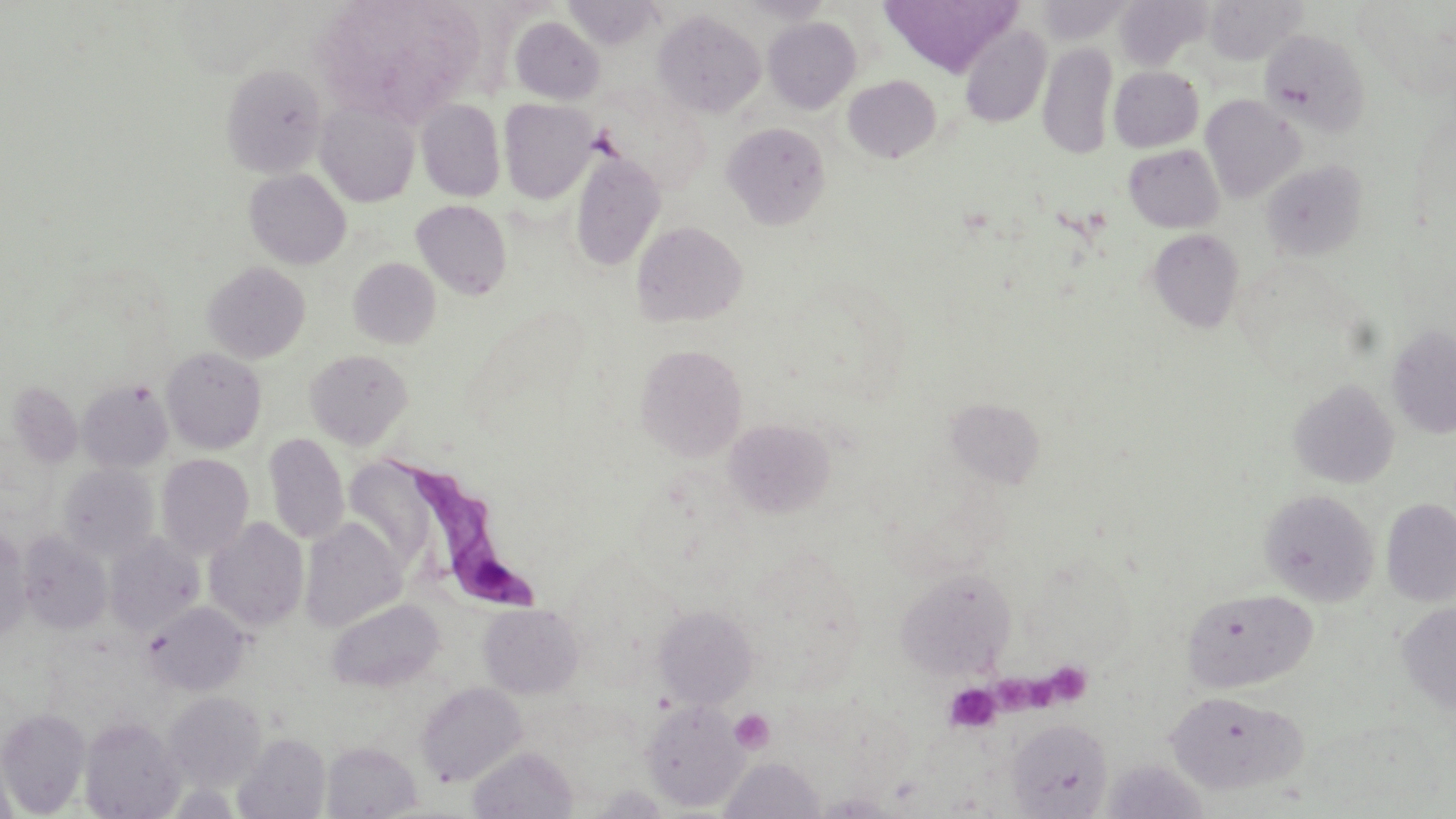
Summary:
  - Coordinate format: approximate bounding boxes as (x1, y1, x2, y2) in pixels
  - Platelet locations: (1052, 671, 1085, 707), (1000, 675, 1063, 725), (943, 683, 1001, 733), (729, 709, 774, 754)
  - Uninfected red blood cell locations: (312, 0, 485, 125), (879, 0, 1021, 77), (1114, 0, 1208, 71), (1205, 0, 1304, 64), (1035, 1, 1131, 43), (653, 10, 766, 118), (509, 16, 605, 104), (763, 17, 861, 113), (959, 23, 1052, 127), (1259, 29, 1371, 138), (1038, 42, 1118, 160), (220, 64, 327, 178), (1109, 66, 1204, 151), (843, 75, 941, 164), (1200, 94, 1306, 203), (315, 99, 420, 207), (416, 99, 505, 201), (499, 99, 598, 203), (722, 122, 831, 230), (1124, 144, 1224, 233), (569, 150, 666, 271), (1261, 160, 1366, 261), (244, 168, 351, 269), (411, 200, 512, 300), (631, 221, 747, 326), (1147, 229, 1244, 333), (349, 257, 441, 349), (203, 261, 311, 362), (1386, 324, 1456, 439), (635, 344, 748, 462), (161, 347, 267, 454), (304, 349, 413, 449), (79, 379, 173, 473), (1288, 379, 1399, 488), (7, 381, 83, 467), (945, 398, 1044, 489), (724, 418, 835, 518), (264, 432, 349, 546), (156, 454, 254, 559), (349, 459, 430, 569), (57, 463, 159, 561), (1259, 489, 1379, 605), (1382, 498, 1456, 607), (204, 517, 309, 631), (300, 517, 406, 632), (0, 531, 31, 639), (18, 532, 112, 634), (105, 532, 204, 636), (895, 568, 1016, 679), (1182, 588, 1317, 693), (326, 598, 444, 692), (144, 601, 250, 695), (1397, 602, 1456, 716), (479, 603, 584, 697), (653, 604, 758, 708), (415, 681, 527, 787), (1165, 689, 1305, 793), (163, 692, 266, 789), (642, 699, 749, 812), (0, 708, 91, 816), (79, 716, 184, 818), (1007, 719, 1113, 818), (234, 732, 331, 819), (322, 742, 421, 818), (468, 745, 577, 819), (719, 757, 826, 818), (1102, 758, 1208, 818), (589, 785, 670, 818), (812, 793, 901, 817)
  - Trypanosoma brucei locations: (394, 458, 554, 614)
  - Slide-level diagnosis: Trypanosoma brucei
  - Preparation: thin blood smear
  - Field of view: one of a larger specimen
  - Image size: 1456×819 pixels
  - Stain: May-Grünwald-Giemsa
  - Modality: optical microscopy
  - Magnification: 1000x